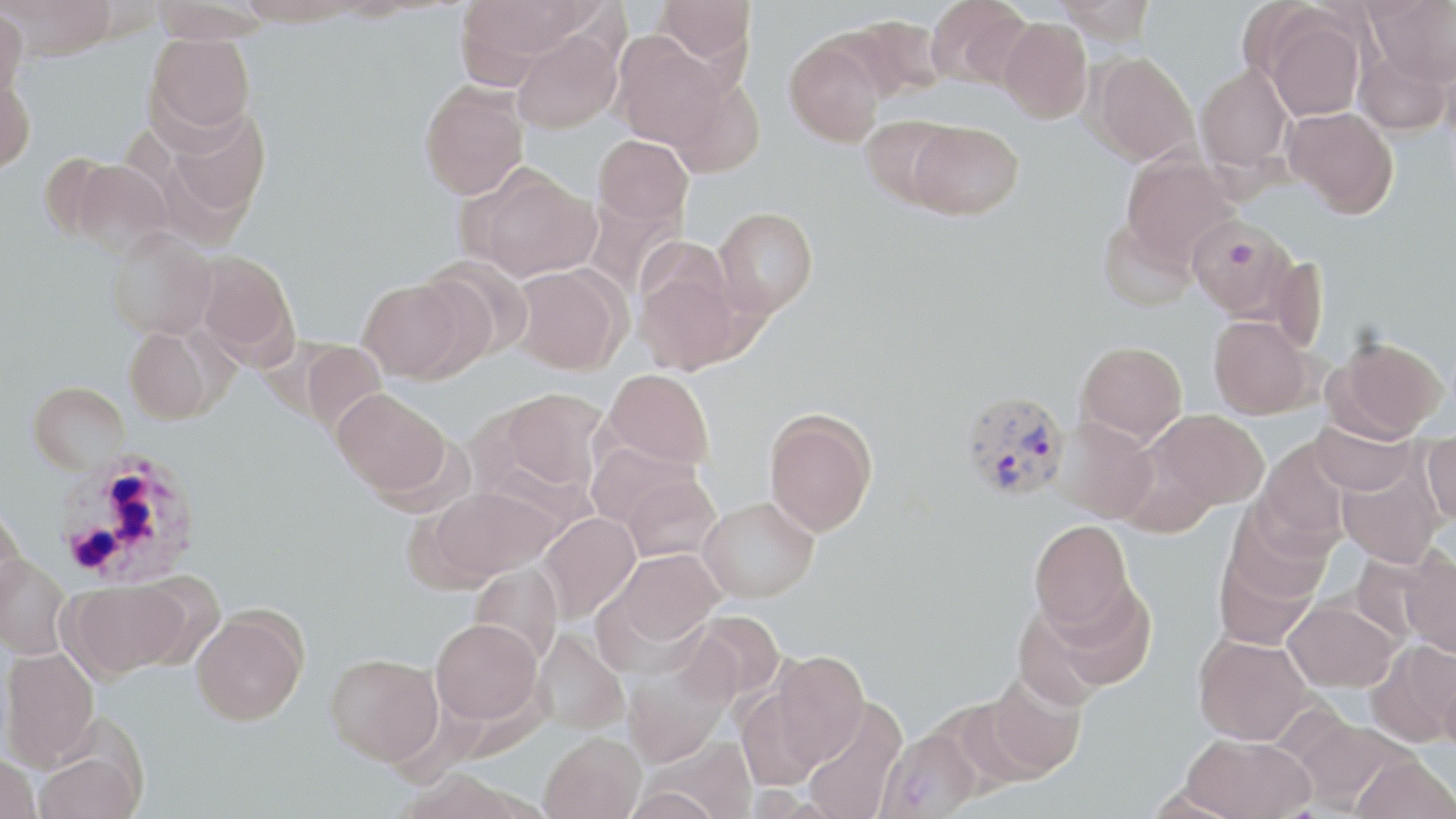
slide-level diagnosis = Plasmodium vivax
modality = optical microscopy
uninfected red blood cell locations = approximate bounding boxes as (x1,y1)-(x2,y2) corner pairs in pixels: (2,0)-(118,60), (150,0)-(273,44), (234,0)-(363,26), (455,0)-(593,75), (657,0)-(755,71), (1055,0)-(1157,45), (1367,0)-(1456,87), (926,1)-(1031,89), (0,4)-(28,106), (1263,13)-(1366,121), (836,16)-(947,104), (998,18)-(1092,123), (510,29)-(622,134), (146,32)-(256,138), (612,34)-(728,152), (784,36)-(886,146), (1354,48)-(1452,136), (1089,51)-(1200,165), (1195,63)-(1294,173), (0,72)-(36,174), (668,72)-(765,177), (419,80)-(530,200), (158,103)-(272,227), (1284,106)-(1398,217), (859,115)-(961,209), (907,120)-(1024,220), (594,134)-(693,228), (38,151)-(123,243), (1121,154)-(1238,266), (67,160)-(175,260), (467,166)-(601,282), (712,206)-(818,319), (1188,215)-(1294,319), (1097,217)-(1198,312), (106,227)-(217,341), (194,251)-(299,365), (632,251)-(752,375), (419,255)-(534,364), (508,264)-(628,375), (356,277)-(478,383), (1208,315)-(1314,419), (124,327)-(214,424), (1327,334)-(1447,443), (296,340)-(388,435), (1076,340)-(1187,446), (601,368)-(715,472), (28,381)-(131,476), (332,388)-(453,498), (494,388)-(610,494), (763,408)-(878,537), (1148,409)-(1268,512), (1309,414)-(1416,496), (1053,417)-(1158,523), (1422,428)-(1456,525), (1255,439)-(1352,550), (586,441)-(708,535), (1335,456)-(1444,568), (611,467)-(723,562), (429,485)-(558,584), (698,497)-(818,603), (0,503)-(28,614), (1220,503)-(1334,608), (537,512)-(641,624), (1029,518)-(1137,636), (1212,535)-(1323,651), (607,548)-(723,647), (1399,548)-(1456,657), (0,555)-(72,659), (468,561)-(564,665), (126,571)-(226,670), (64,579)-(186,679), (1024,581)-(1155,700), (1283,598)-(1400,692), (191,609)-(308,726), (678,612)-(785,709), (431,618)-(543,724), (532,628)-(629,735), (1193,635)-(1315,745), (1366,640)-(1456,748), (2,646)-(100,768), (766,650)-(870,771), (325,652)-(443,765), (621,661)-(730,768), (977,671)-(1088,781), (801,698)-(907,819), (1290,716)-(1411,813), (876,728)-(982,818), (540,731)-(646,819), (1181,733)-(1315,819), (646,736)-(758,819), (33,742)-(145,819), (1351,753)-(1456,819), (0,754)-(41,819)
Plasmodium vivax-infected red blood cell locations = approximate bounding boxes as (x1,y1)-(x2,y2) corner pairs in pixels: (959,390)-(1071,503), (58,450)-(201,588)
stain = May-Grünwald-Giemsa
preparation = thin blood film
image size = 1456×819 pixels
field of view = one of a larger specimen
magnification = 1000x